Assess this cell for malaria.
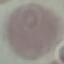

Uninfected.

{
  "capture": "smartphone camera at the microscope eyepiece",
  "preparation": "thin blood film",
  "image_type": "automatically extracted cell patch, resized to 64 × 64 pixels",
  "stain": "Giemsa"
}